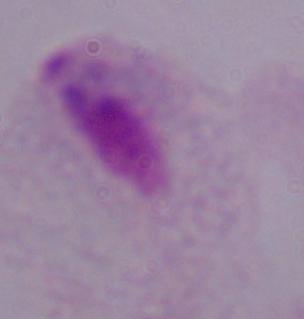
Summary:
  - Identification: trichomonad
  - Modality: photomicrograph
  - Magnification: 1000x